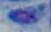

modality = photomicrograph
identification = Toxoplasma gondii
magnification = 1000x